Assess this cell for malaria.
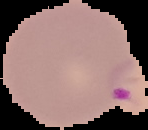

It is parasitized.

image size = 148×130 pixels
preparation = thin blood smear
image type = segmented cell region on a black background